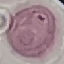

malaria status = uninfected
capture = smartphone camera at the microscope eyepiece
stain = Giemsa
image type = cell patch, automatically extracted from a larger field of view and resized to 64 × 64 pixels
preparation = thin blood smear